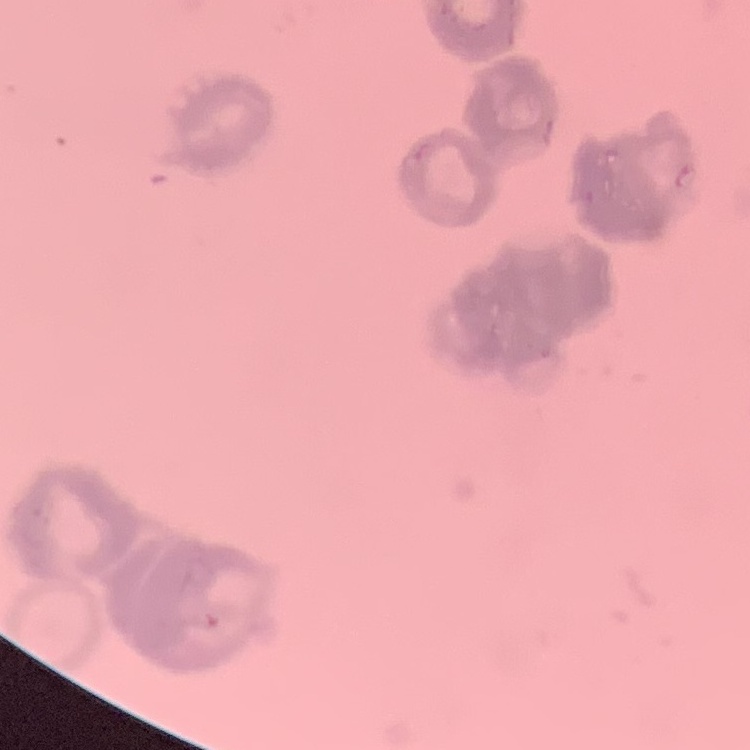

red blood cell morphology = rouleaux formation
preparation = thin blood smear
stain = Field's or Giemsa
image type = one tile cut from a larger photomicrograph